Locate every blood parasite and identify its species.
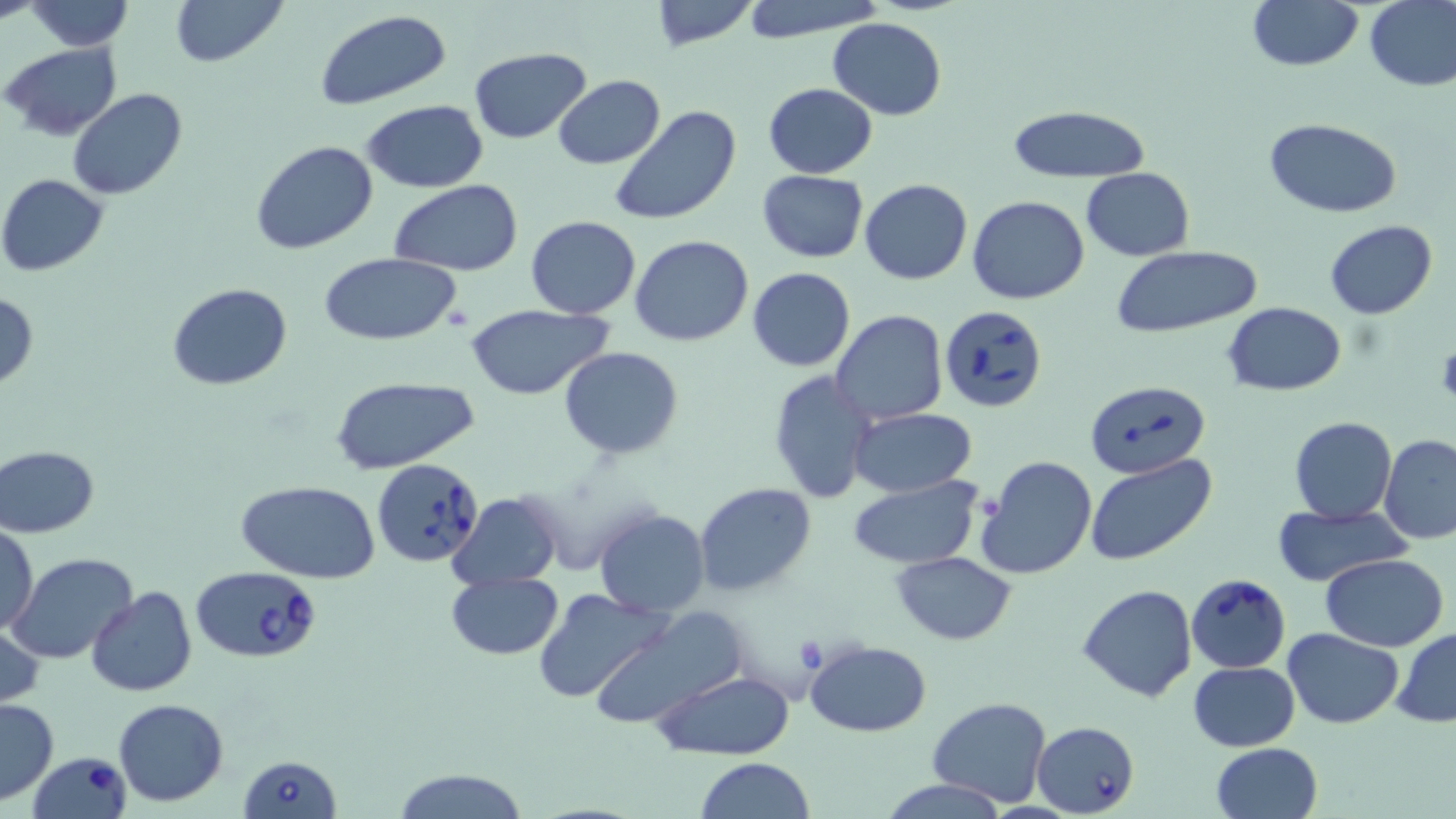
Approximate bounding boxes as (x1,y1)-(x2,y2) corner pairs in pixels.
Babesia divergens-infected red blood cells: (939,305)-(1045,414), (1085,379)-(1208,476), (370,457)-(483,567), (190,565)-(323,663), (1187,573)-(1290,672), (1032,721)-(1139,816), (27,750)-(131,819), (238,754)-(341,819).
No Plasmodium falciparum, Plasmodium ovale, Plasmodium malariae, Plasmodium vivax, or Trypanosoma brucei observed.

Uninfected red blood cell locations: (24,0)-(133,51), (168,0)-(289,68), (738,0)-(887,42), (1247,0)-(1364,72), (1363,0)-(1456,92), (648,1)-(760,51), (314,9)-(451,111), (828,16)-(946,121), (2,42)-(123,141), (468,48)-(591,144), (553,76)-(665,169), (763,83)-(878,178), (68,88)-(189,201), (361,99)-(489,194), (611,104)-(742,228), (1009,106)-(1152,183), (1264,117)-(1402,218), (251,140)-(380,255), (1082,168)-(1195,260), (757,171)-(868,262), (0,174)-(108,275), (861,179)-(972,286), (390,180)-(522,274), (969,196)-(1091,304), (525,216)-(642,318), (1325,219)-(1437,319), (630,236)-(754,347), (1109,246)-(1263,338), (319,253)-(463,343), (748,267)-(856,371), (167,283)-(293,389), (0,292)-(39,391), (1223,303)-(1347,395), (462,304)-(616,398), (831,310)-(948,424), (559,347)-(684,459), (769,370)-(878,504), (328,374)-(482,475), (849,407)-(979,498), (1289,416)-(1397,524), (1379,433)-(1456,543), (1,445)-(99,537), (1087,455)-(1215,567), (976,456)-(1097,580), (846,475)-(982,570), (238,480)-(380,582), (696,483)-(817,598), (448,490)-(563,591), (1274,504)-(1406,586), (593,508)-(709,617), (0,521)-(38,632), (7,551)-(139,664), (891,551)-(1017,645), (1320,554)-(1450,651), (444,571)-(564,659), (1078,584)-(1199,701), (87,587)-(197,696), (534,589)-(672,705), (584,608)-(749,731), (1,618)-(47,710), (1392,626)-(1456,728), (1282,629)-(1404,727), (804,640)-(931,737), (1189,661)-(1299,752), (650,668)-(795,761), (928,697)-(1052,805), (0,698)-(58,804), (113,698)-(230,806), (1211,743)-(1322,818), (697,757)-(816,818), (388,766)-(530,819), (878,778)-(1007,817). Slide-level diagnosis: Babesia divergens. May-Grünwald-Giemsa stain. Image is 1456×819 pixels. Optical microscopy. Thin blood smear. Single field of view. 1000x magnification.